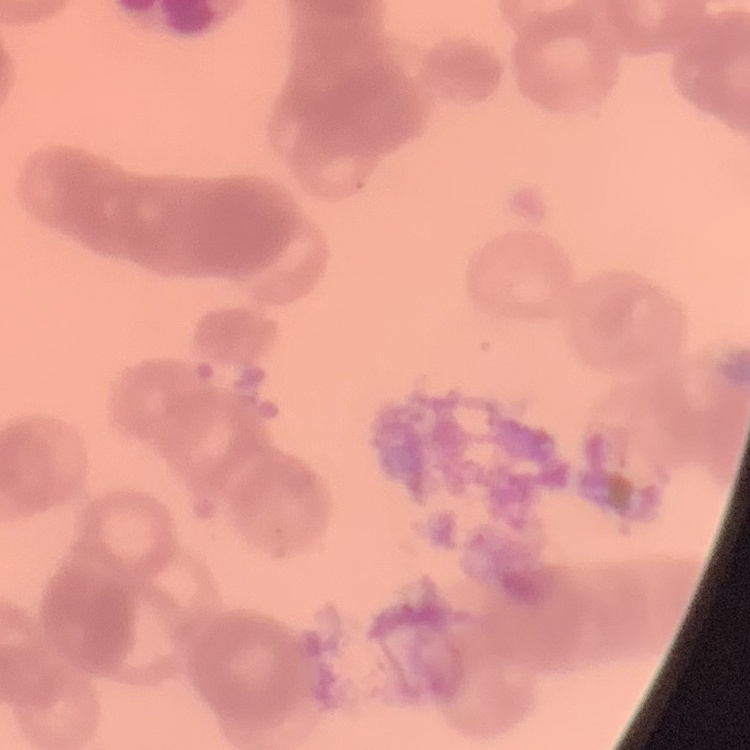

The erythrocytes exhibit rouleaux formation. One tile cut from a larger photomicrograph. Thin peripheral smear. Stained with either Field's or Giemsa.